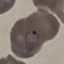
result = malaria parasites detected
stain = Giemsa
image type = automatically extracted cell patch, resized to 64 × 64 pixels
preparation = thin blood film
capture = smartphone through the microscope eyepiece